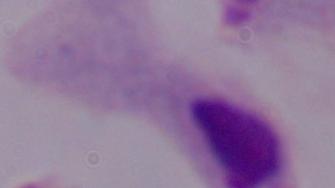
identification = trichomonad
modality = micrograph
magnification = 1000x